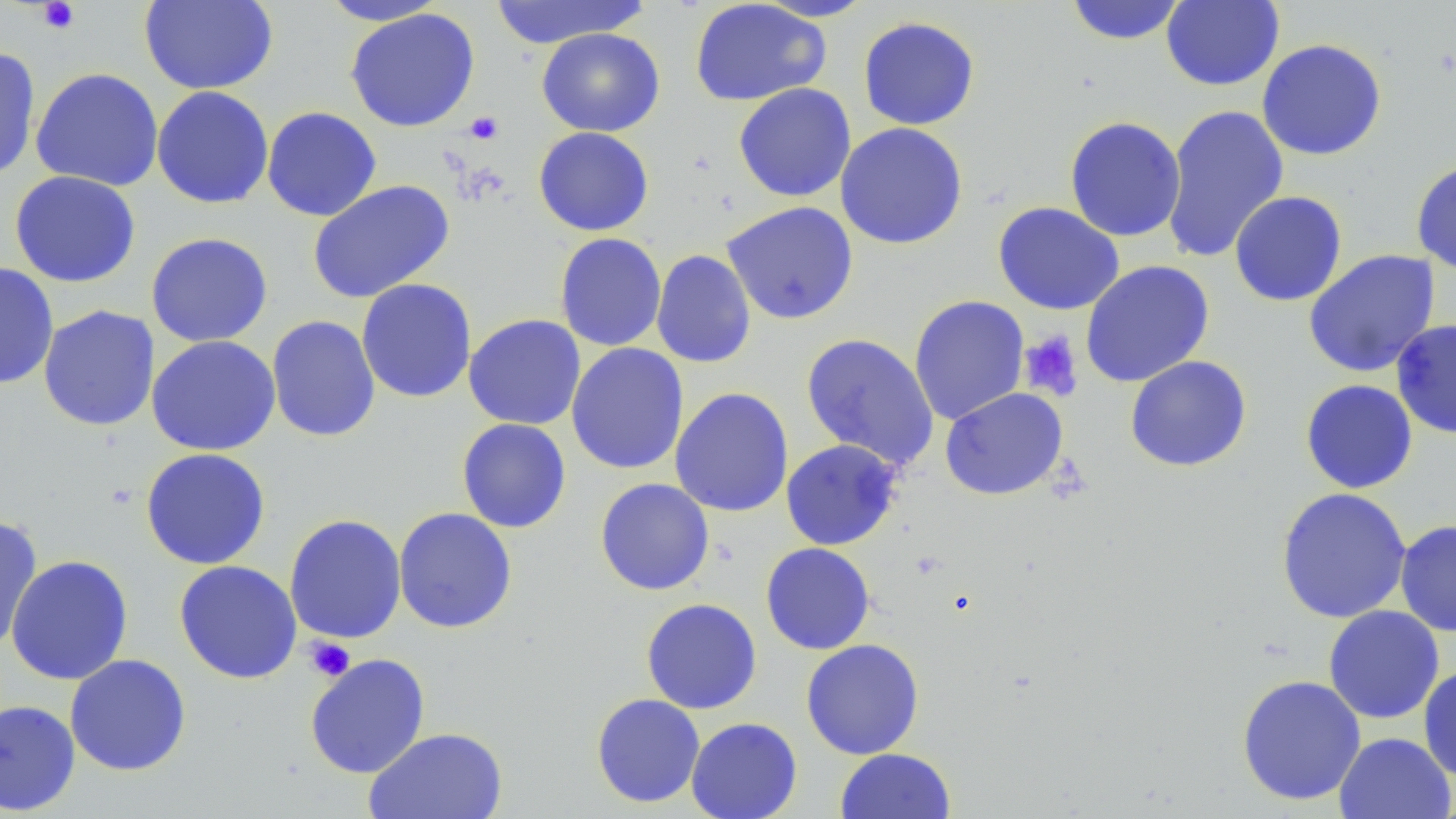
Approximate bounding boxes as (x1, y1, x2, y2) in pixels. Platelet locations: (36, 1, 81, 34), (464, 112, 504, 145), (1018, 330, 1083, 401), (305, 636, 356, 681). Uninfected red blood cell locations: (138, 0, 278, 95), (316, 0, 451, 26), (487, 0, 651, 47), (753, 0, 877, 22), (1065, 0, 1188, 45), (1160, 0, 1284, 91), (689, 1, 831, 106), (344, 7, 481, 132), (858, 16, 980, 130), (537, 28, 665, 137), (1256, 38, 1388, 161), (0, 46, 41, 182), (30, 67, 164, 192), (733, 83, 856, 202), (151, 86, 274, 209), (1161, 105, 1289, 263), (262, 106, 382, 221), (1064, 116, 1186, 242), (834, 122, 968, 249), (533, 126, 654, 236), (1410, 160, 1456, 275), (9, 170, 141, 288), (307, 179, 455, 304), (1229, 191, 1347, 307), (720, 201, 859, 325), (992, 201, 1125, 315), (145, 231, 273, 348), (554, 233, 667, 352), (651, 249, 757, 369), (1303, 249, 1441, 378), (1080, 260, 1215, 387), (0, 262, 59, 390), (355, 277, 476, 403), (908, 295, 1030, 426), (355, 300, 585, 414), (38, 305, 159, 431), (463, 313, 586, 430), (266, 315, 381, 442), (1390, 318, 1456, 440), (801, 332, 940, 472), (146, 335, 282, 456), (566, 342, 689, 475), (1125, 355, 1253, 473), (1299, 379, 1418, 494), (670, 387, 794, 517), (940, 387, 1068, 501), (456, 418, 572, 533), (780, 439, 902, 551), (139, 447, 271, 570), (595, 478, 714, 595), (1275, 487, 1412, 624), (393, 507, 518, 634), (284, 514, 407, 644), (0, 515, 43, 654), (1394, 519, 1456, 637), (760, 542, 876, 655), (5, 554, 133, 685), (173, 560, 302, 684), (641, 598, 762, 714), (1323, 605, 1445, 724), (800, 639, 925, 760), (304, 653, 430, 779), (64, 654, 191, 776), (1417, 664, 1456, 782), (1236, 674, 1366, 806), (591, 693, 705, 808), (0, 698, 81, 815), (685, 717, 802, 819), (364, 727, 508, 819), (1333, 732, 1455, 819), (835, 748, 957, 819). Slide-level diagnosis: no evidence of blood parasites. Single field of view. Thin blood smear. May-Grünwald-Giemsa-stained preparation. Image is 1456×819 pixels. Light microscopy. 1000x magnification.